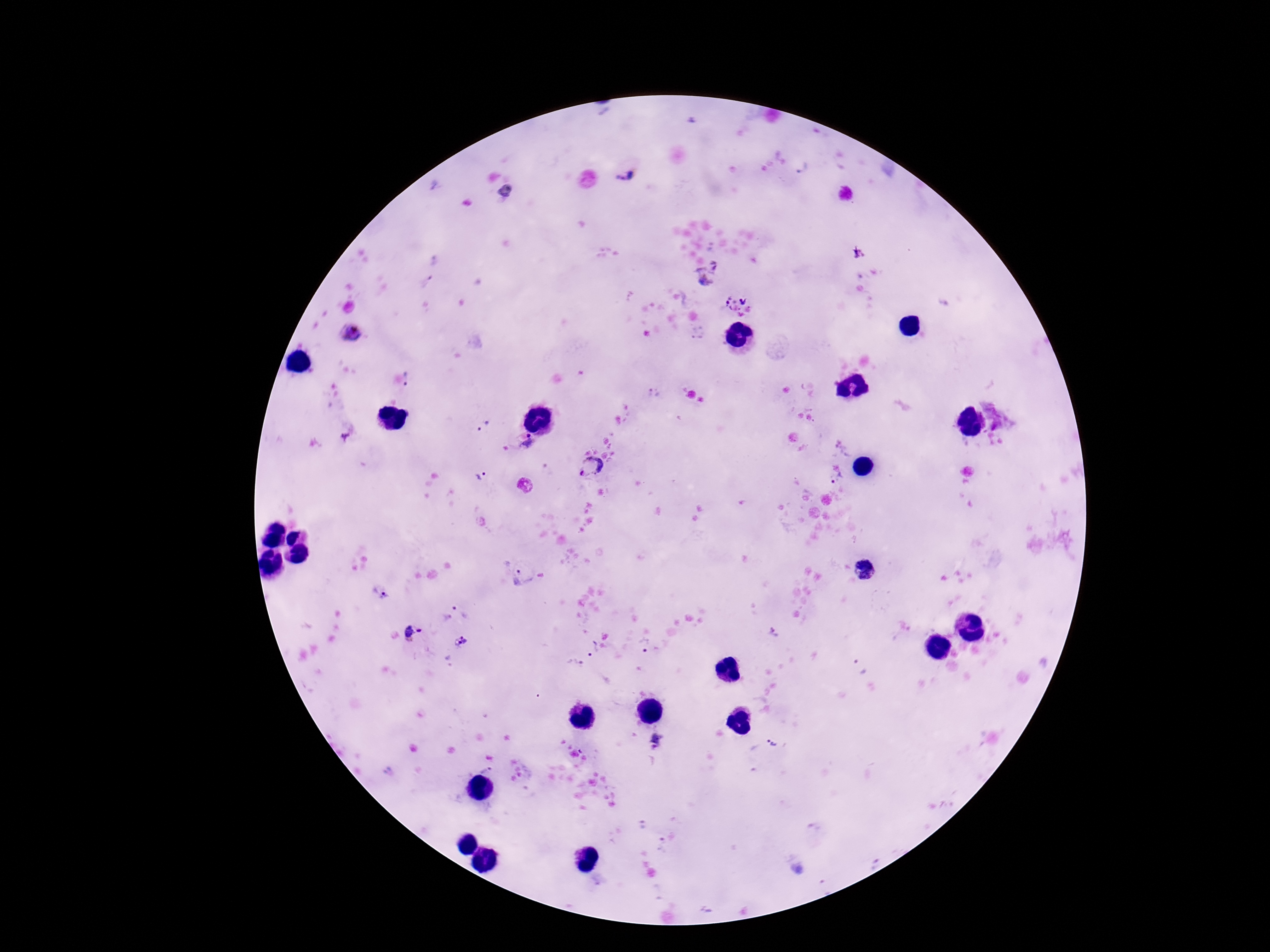

Approximate object centers, in pixels from the top-left corner.
Summary:
  - Plasmodium parasite locations: (x=804, y=170), (x=623, y=177), (x=716, y=265), (x=432, y=268), (x=704, y=279), (x=745, y=300), (x=352, y=332), (x=409, y=380), (x=483, y=427), (x=344, y=437), (x=530, y=442), (x=591, y=467), (x=480, y=475), (x=836, y=480), (x=524, y=486), (x=865, y=570), (x=523, y=575), (x=380, y=594), (x=461, y=610), (x=420, y=631), (x=408, y=632), (x=460, y=641), (x=647, y=646), (x=592, y=647), (x=575, y=665), (x=858, y=666), (x=656, y=742), (x=773, y=744), (x=486, y=769), (x=641, y=827), (x=662, y=846), (x=875, y=864)
  - Capture: smartphone camera through the microscope eyepiece
  - Patient malaria status: positive
  - Image size: 1270×952 pixels
  - Preparation: thick blood film
  - Stain: Giemsa
  - Magnification: 100x
  - Field of view: single